Point out each Plasmodium parasite.
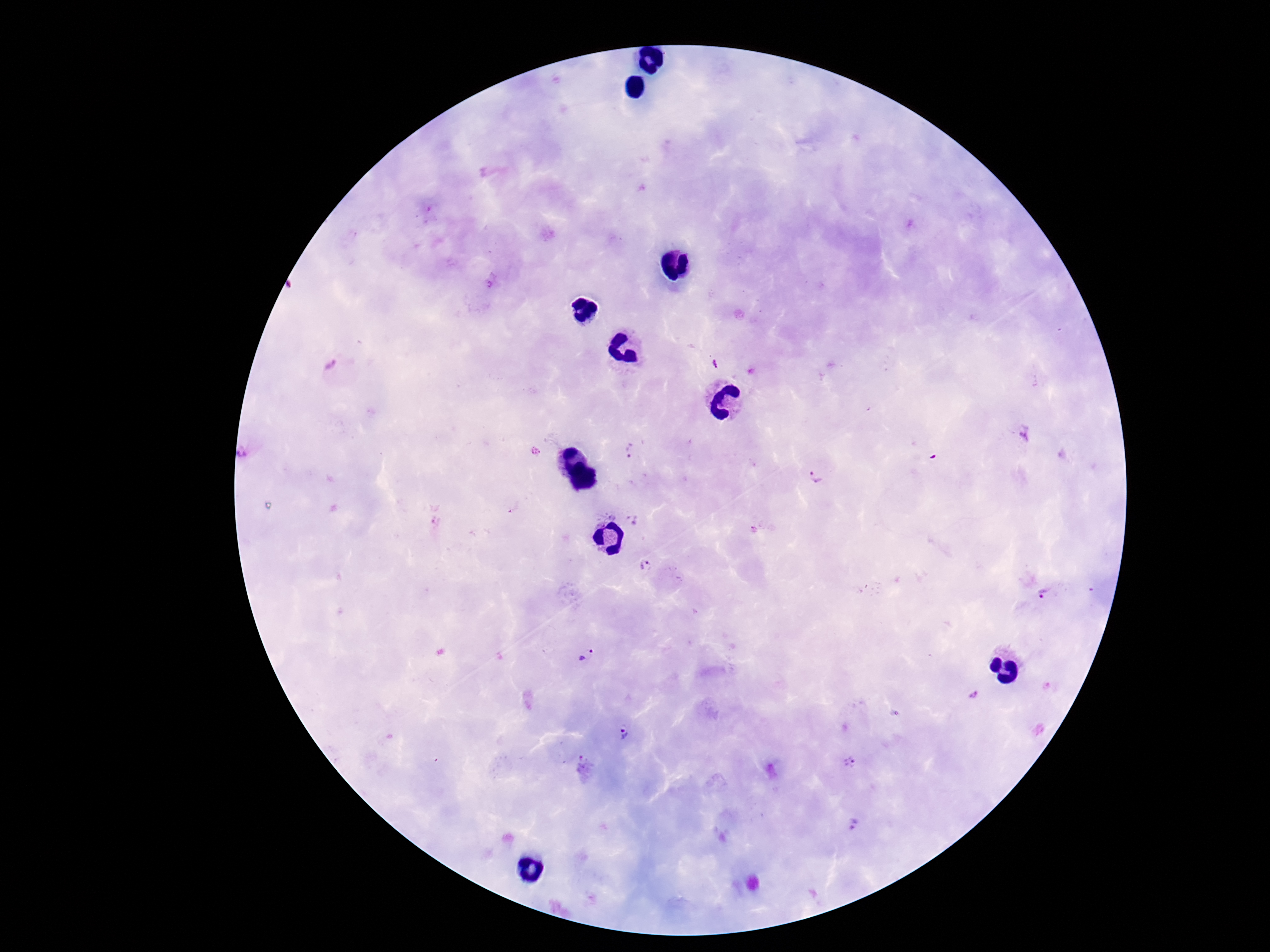
Approximate centers as {x, y} in pixels.
Plasmodium parasites: {715, 364}, {335, 372}, {1025, 432}, {248, 451}, {631, 451}, {816, 475}, {611, 514}, {597, 521}, {635, 521}, {644, 564}, {1044, 595}, {586, 656}, {972, 695}, {626, 734}, {850, 762}, {855, 823}.

Smartphone photograph taken through the microscope eyepiece. Patient malaria status: infected. 100x magnification. Thick blood smear. Image is 1270×952 pixels. Giemsa-stained preparation. One field from this slide.